Classify this cell by malaria status.
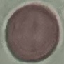

It is uninfected.

Photographed with a smartphone camera at the microscope eyepiece. Thin blood film. Cell patch, automatically extracted from a larger field of view and resized to 64 × 64 pixels. Giemsa-stained preparation.